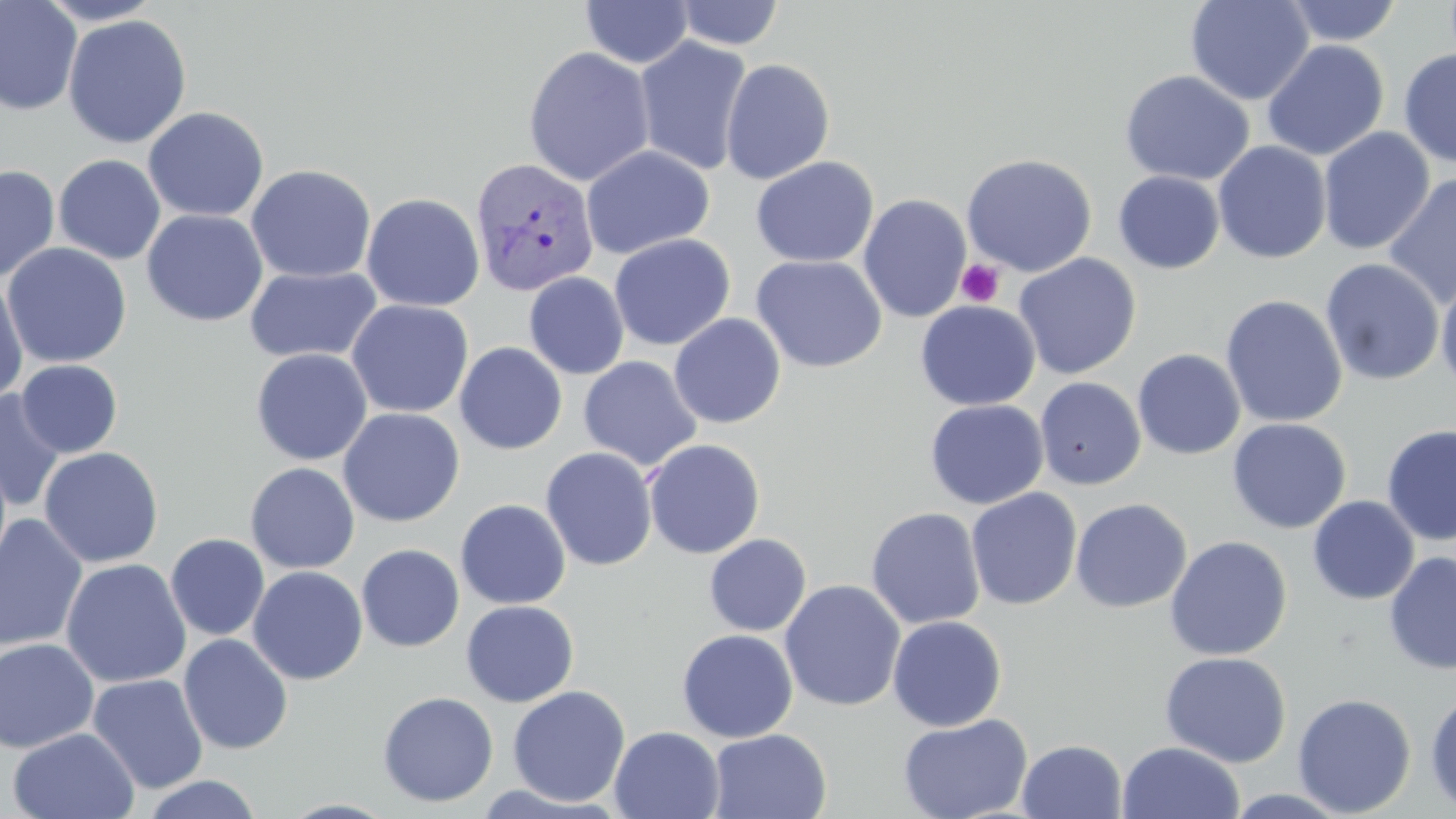
slide_level_diagnosis: Plasmodium vivax
uninfected_red_blood_cell_locations: 'approximate bounding boxes as named x1/y1/x2/y2 corners in pixels: (x1=1185, y1=0, x2=1314, y2=105), (x1=1281, y1=0, x2=1403, y2=46), (x1=0, y1=1, x2=83, y2=116), (x1=580, y1=1, x2=694, y2=69), (x1=672, y1=1, x2=784, y2=50), (x1=62, y1=14, x2=193, y2=149), (x1=633, y1=36, x2=753, y2=176), (x1=1262, y1=39, x2=1389, y2=161), (x1=522, y1=46, x2=656, y2=186), (x1=1398, y1=47, x2=1456, y2=168), (x1=720, y1=58, x2=836, y2=184), (x1=1119, y1=69, x2=1255, y2=186), (x1=143, y1=105, x2=269, y2=222), (x1=1317, y1=127, x2=1435, y2=255), (x1=1212, y1=140, x2=1332, y2=264), (x1=580, y1=145, x2=715, y2=260), (x1=961, y1=153, x2=1098, y2=277), (x1=53, y1=154, x2=166, y2=265), (x1=751, y1=156, x2=879, y2=268), (x1=246, y1=163, x2=376, y2=283), (x1=0, y1=164, x2=60, y2=283), (x1=1113, y1=170, x2=1225, y2=274), (x1=1383, y1=173, x2=1456, y2=309), (x1=361, y1=192, x2=486, y2=312), (x1=858, y1=193, x2=972, y2=323), (x1=141, y1=209, x2=268, y2=326), (x1=609, y1=234, x2=735, y2=351), (x1=1, y1=242, x2=133, y2=369), (x1=750, y1=254, x2=887, y2=373), (x1=1012, y1=254, x2=1141, y2=380), (x1=1320, y1=258, x2=1444, y2=386), (x1=244, y1=265, x2=383, y2=364), (x1=1435, y1=270, x2=1456, y2=396), (x1=523, y1=272, x2=629, y2=380), (x1=0, y1=276, x2=29, y2=406), (x1=1220, y1=294, x2=1348, y2=428), (x1=346, y1=299, x2=474, y2=419), (x1=915, y1=300, x2=1041, y2=411), (x1=669, y1=313, x2=786, y2=429), (x1=454, y1=342, x2=567, y2=455), (x1=250, y1=348, x2=373, y2=466), (x1=1132, y1=348, x2=1246, y2=460), (x1=578, y1=356, x2=701, y2=471), (x1=16, y1=359, x2=123, y2=457), (x1=1034, y1=377, x2=1146, y2=490), (x1=0, y1=390, x2=66, y2=511), (x1=925, y1=399, x2=1049, y2=509), (x1=338, y1=407, x2=464, y2=527), (x1=1227, y1=418, x2=1351, y2=534), (x1=1381, y1=424, x2=1456, y2=545), (x1=643, y1=438, x2=766, y2=559), (x1=39, y1=446, x2=164, y2=568), (x1=540, y1=447, x2=657, y2=571), (x1=245, y1=462, x2=360, y2=574), (x1=966, y1=487, x2=1082, y2=610), (x1=1307, y1=495, x2=1419, y2=605), (x1=1070, y1=497, x2=1192, y2=613), (x1=455, y1=499, x2=571, y2=609), (x1=865, y1=507, x2=986, y2=629), (x1=0, y1=514, x2=88, y2=653), (x1=165, y1=533, x2=270, y2=640), (x1=704, y1=534, x2=811, y2=636), (x1=1165, y1=535, x2=1292, y2=661), (x1=357, y1=544, x2=465, y2=652), (x1=1384, y1=551, x2=1456, y2=674), (x1=61, y1=558, x2=192, y2=688), (x1=248, y1=566, x2=368, y2=684), (x1=779, y1=579, x2=906, y2=712), (x1=460, y1=600, x2=579, y2=707), (x1=887, y1=615, x2=1007, y2=732), (x1=677, y1=629, x2=798, y2=743), (x1=178, y1=633, x2=293, y2=754), (x1=0, y1=637, x2=99, y2=753), (x1=1160, y1=651, x2=1291, y2=767), (x1=87, y1=674, x2=209, y2=794), (x1=507, y1=685, x2=631, y2=807), (x1=1424, y1=689, x2=1456, y2=815), (x1=377, y1=691, x2=499, y2=808), (x1=1292, y1=693, x2=1417, y2=817), (x1=898, y1=713, x2=1032, y2=819), (x1=609, y1=726, x2=725, y2=819), (x1=7, y1=727, x2=138, y2=818), (x1=708, y1=729, x2=832, y2=818), (x1=1017, y1=740, x2=1127, y2=819), (x1=1117, y1=741, x2=1246, y2=819), (x1=140, y1=774, x2=263, y2=818)'
field_of_view: one of a larger specimen
platelet_locations: 'approximate bounding boxes as named x1/y1/x2/y2 corners in pixels: (x1=956, y1=259, x2=1005, y2=307)'
plasmodium_vivax_infected_red_blood_cell_locations: 'approximate bounding boxes as named x1/y1/x2/y2 corners in pixels: (x1=469, y1=157, x2=598, y2=297)'
image_size: 1456×819 pixels
stain: May-Grünwald-Giemsa
magnification: 1000x
preparation: thin blood film
modality: optical microscopy